Identify the parasite.
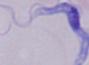
A trypanosome.

Summary:
  - Modality: micrograph
  - Magnification: 1000x